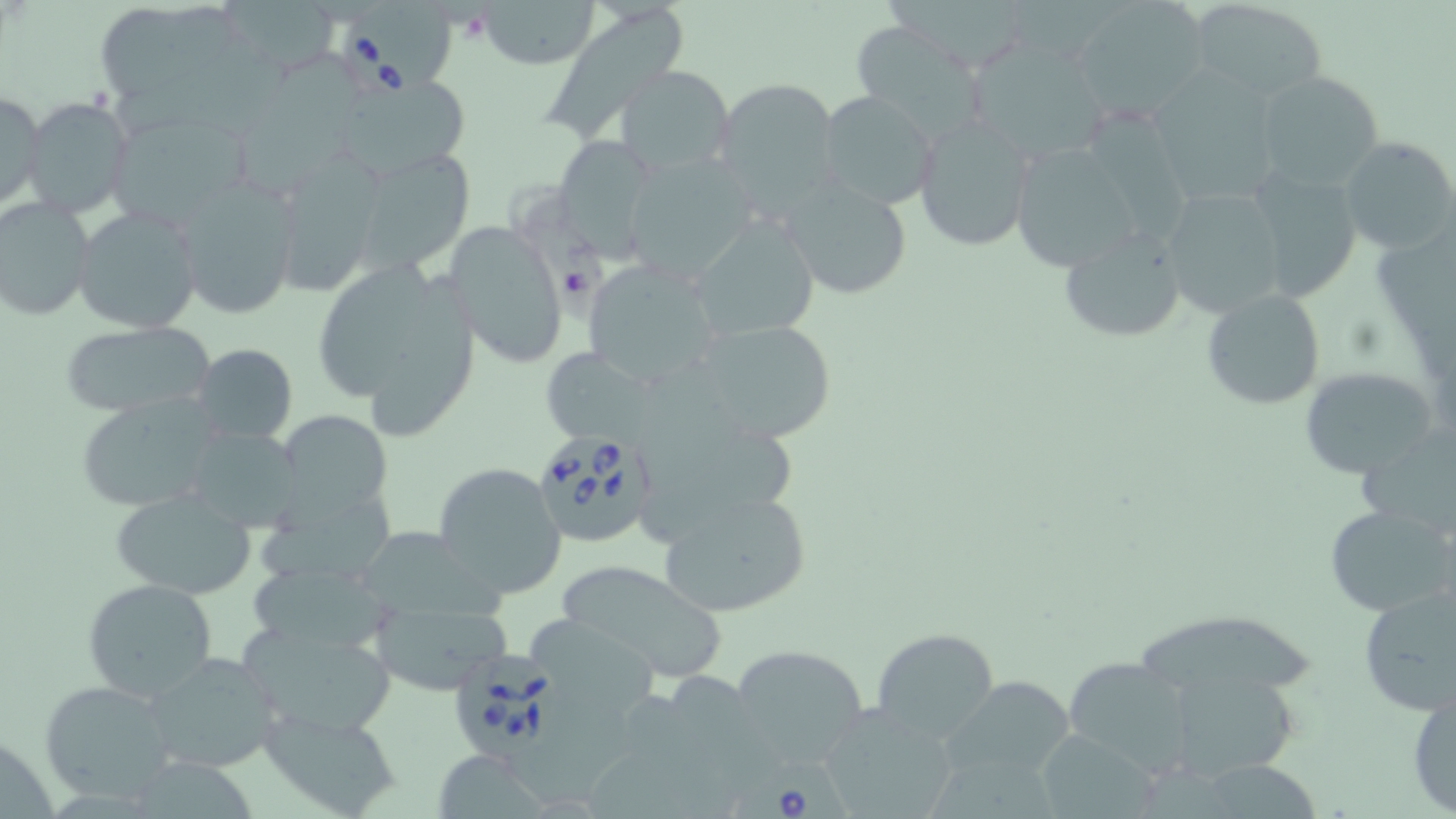

Approximate bounding boxes as named x1/y1/x2/y2 corners in pixels. Babesia divergens-infected red blood cell locations: (x1=340, y1=17, x2=436, y2=107), (x1=510, y1=189, x2=607, y2=327), (x1=530, y1=430, x2=660, y2=550), (x1=447, y1=650, x2=560, y2=760), (x1=730, y1=755, x2=855, y2=819). Uninfected red blood cell locations: (x1=231, y1=0, x2=341, y2=76), (x1=475, y1=0, x2=597, y2=71), (x1=886, y1=0, x2=1035, y2=69), (x1=1190, y1=0, x2=1326, y2=100), (x1=1070, y1=1, x2=1213, y2=121), (x1=542, y1=6, x2=683, y2=149), (x1=98, y1=7, x2=205, y2=98), (x1=847, y1=19, x2=989, y2=135), (x1=244, y1=49, x2=374, y2=191), (x1=972, y1=49, x2=1107, y2=156), (x1=616, y1=64, x2=735, y2=179), (x1=1152, y1=68, x2=1276, y2=204), (x1=1253, y1=69, x2=1386, y2=190), (x1=337, y1=72, x2=471, y2=177), (x1=712, y1=76, x2=846, y2=218), (x1=1, y1=90, x2=45, y2=213), (x1=816, y1=91, x2=939, y2=210), (x1=25, y1=96, x2=135, y2=220), (x1=912, y1=112, x2=1037, y2=253), (x1=107, y1=113, x2=247, y2=229), (x1=1092, y1=115, x2=1190, y2=243), (x1=550, y1=135, x2=662, y2=259), (x1=1004, y1=135, x2=1151, y2=274), (x1=1339, y1=137, x2=1455, y2=256), (x1=268, y1=145, x2=391, y2=300), (x1=358, y1=147, x2=483, y2=272), (x1=620, y1=153, x2=758, y2=280), (x1=1243, y1=165, x2=1364, y2=304), (x1=170, y1=171, x2=302, y2=318), (x1=780, y1=176, x2=914, y2=300), (x1=1158, y1=185, x2=1289, y2=318), (x1=0, y1=196, x2=95, y2=321), (x1=72, y1=206, x2=202, y2=334), (x1=687, y1=214, x2=819, y2=341), (x1=443, y1=218, x2=570, y2=369), (x1=1056, y1=228, x2=1187, y2=345), (x1=581, y1=255, x2=724, y2=389), (x1=315, y1=256, x2=483, y2=437), (x1=1200, y1=289, x2=1325, y2=410), (x1=687, y1=317, x2=841, y2=445), (x1=57, y1=322, x2=215, y2=417), (x1=190, y1=342, x2=297, y2=445), (x1=539, y1=346, x2=656, y2=445), (x1=1299, y1=365, x2=1438, y2=477), (x1=74, y1=395, x2=227, y2=513), (x1=281, y1=410, x2=396, y2=523), (x1=179, y1=426, x2=305, y2=534), (x1=1355, y1=427, x2=1456, y2=532), (x1=431, y1=461, x2=566, y2=599), (x1=253, y1=481, x2=400, y2=586), (x1=108, y1=488, x2=260, y2=599), (x1=661, y1=491, x2=812, y2=619), (x1=1324, y1=504, x2=1456, y2=617), (x1=370, y1=529, x2=519, y2=629), (x1=556, y1=557, x2=726, y2=681), (x1=249, y1=567, x2=401, y2=655), (x1=81, y1=578, x2=220, y2=703), (x1=1355, y1=583, x2=1456, y2=715), (x1=366, y1=597, x2=515, y2=696), (x1=526, y1=615, x2=658, y2=708), (x1=1135, y1=616, x2=1316, y2=696), (x1=233, y1=617, x2=400, y2=737), (x1=871, y1=628, x2=1000, y2=743), (x1=731, y1=643, x2=869, y2=765), (x1=143, y1=651, x2=283, y2=773), (x1=1065, y1=655, x2=1198, y2=778), (x1=1176, y1=670, x2=1292, y2=773), (x1=943, y1=673, x2=1079, y2=786), (x1=669, y1=674, x2=802, y2=799), (x1=40, y1=679, x2=177, y2=806), (x1=1408, y1=682, x2=1455, y2=816), (x1=518, y1=693, x2=637, y2=806), (x1=818, y1=704, x2=962, y2=817), (x1=259, y1=708, x2=404, y2=818), (x1=1044, y1=729, x2=1157, y2=819), (x1=437, y1=748, x2=544, y2=819), (x1=934, y1=758, x2=1053, y2=819), (x1=1202, y1=761, x2=1314, y2=819). Slide-level diagnosis: Babesia divergens. 1000x magnification. Image is 1456×819 pixels. Light microscopy. May-Grünwald-Giemsa stain. One field of a larger specimen. Thin blood smear.